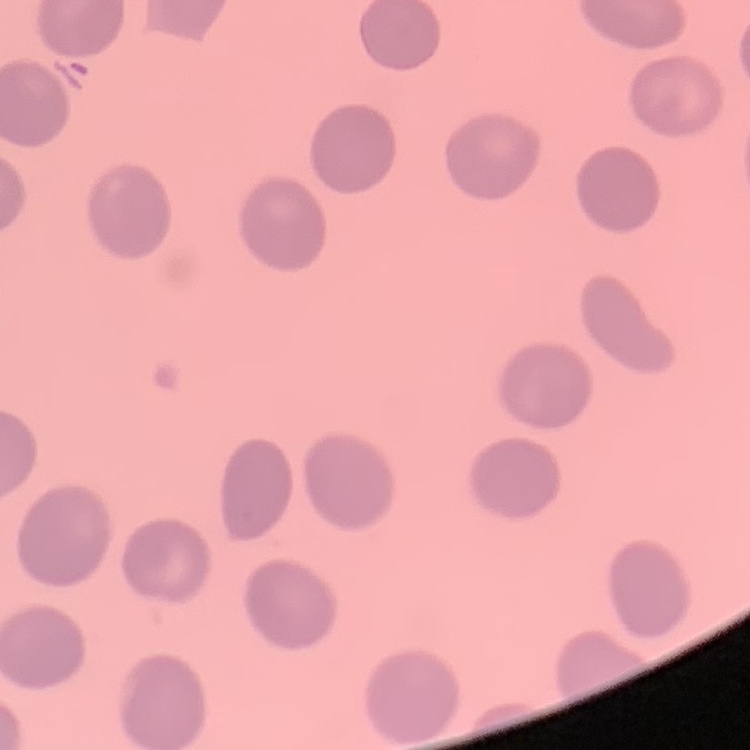
Summary:
  - Erythrocyte morphology: no rouleaux formation
  - Stain: Field's or Giemsa
  - Preparation: thin blood film
  - Image type: square crop of a larger photomicrograph